Classify this cell by malaria status.
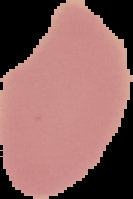
Uninfected.

From a thin blood film. Image is 133×199 pixels. The area outside the segmented cell region is set to black.